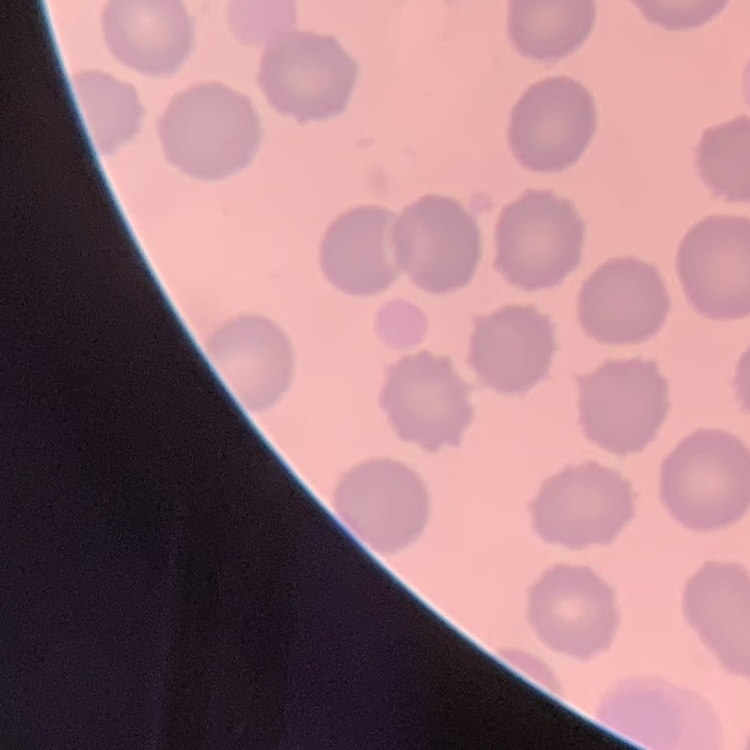
Summary:
  - Erythrocyte morphology: no rouleaux formation
  - Stain: Field's or Giemsa
  - Preparation: thin blood film
  - Image type: square crop of a larger photomicrograph